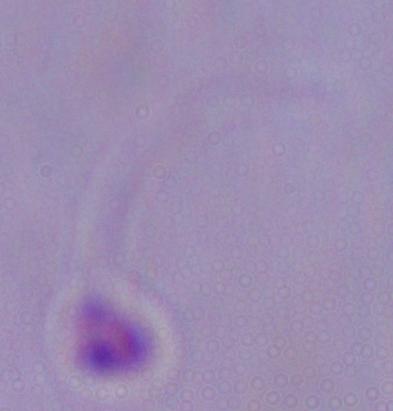
A Leishmania parasite is shown. Micrograph. Captured at 1000x magnification.